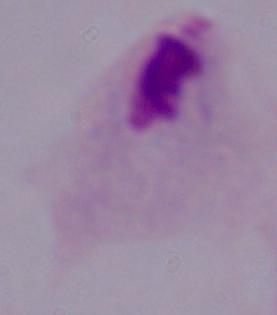 Captured at 1000x magnification. Micrograph. A trichomonad is shown.